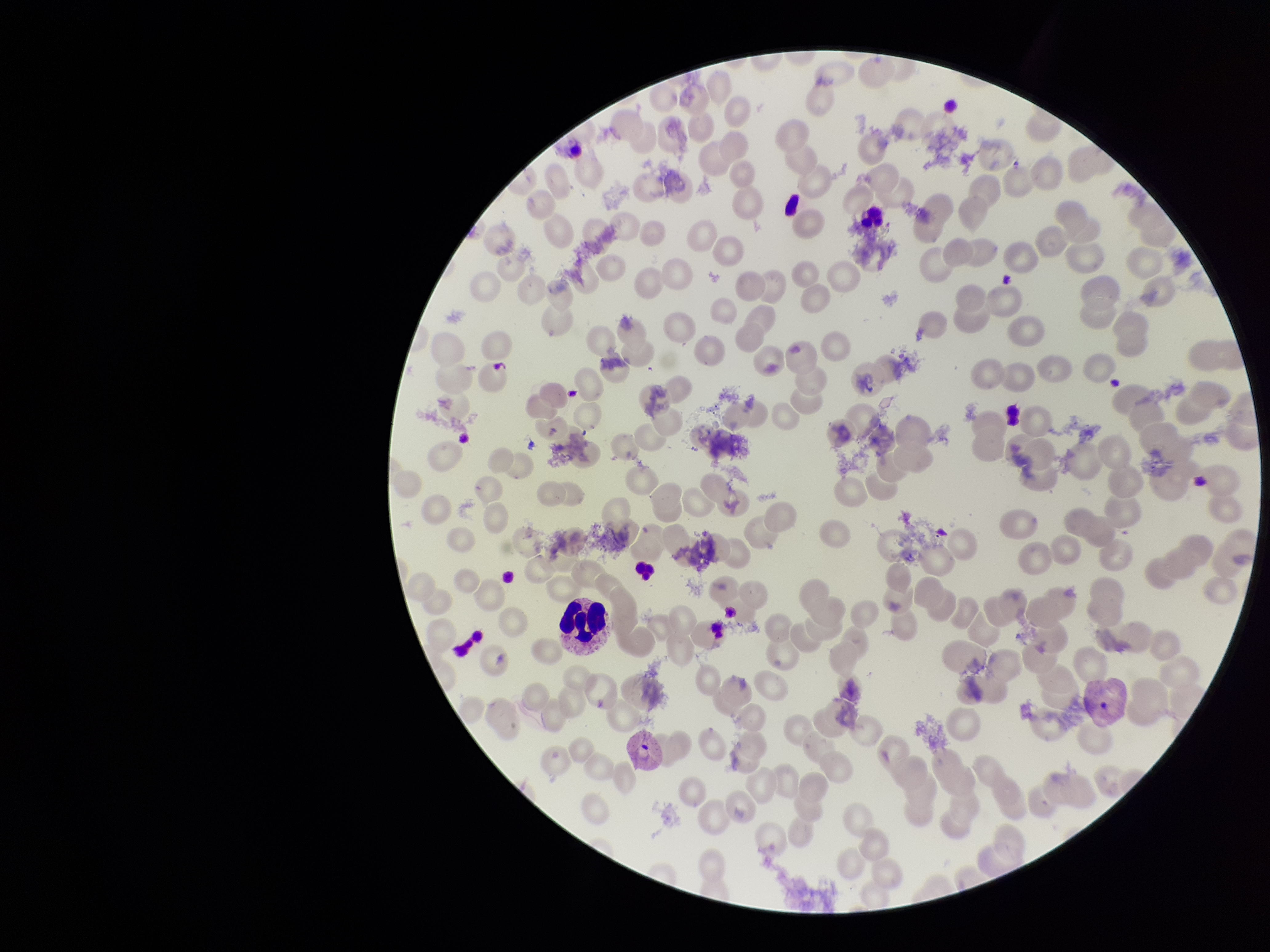
parasitized_red_blood_cell_count: 0
parasitized_red_blood_cells: none seen
species_reported_for_this_patient: Plasmodium vivax
patient_malaria_status: positive
preparation: thin smear
image_size: 1270×952 pixels
red_blood_cell_count: 194
stain: Giemsa
field_of_view: single
capture: smartphone photograph through the microscope eyepiece